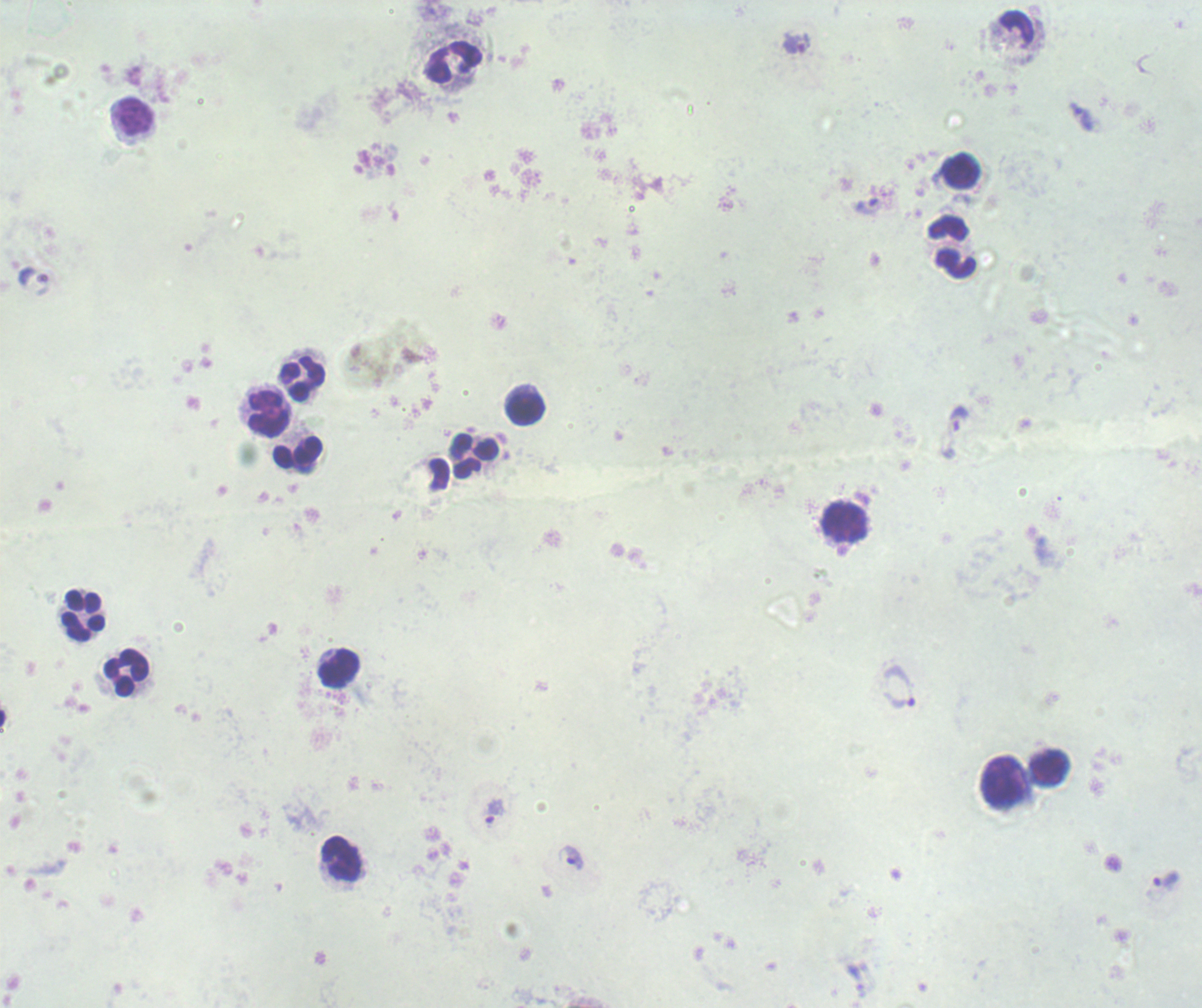

Approximate centers as {x, y} in pixels.
Summary:
  - Leukocyte locations: {453, 62}, {135, 114}, {961, 171}, {949, 228}, {956, 264}, {303, 379}, {526, 409}, {269, 412}, {298, 453}, {476, 455}, {846, 520}, {82, 614}, {339, 668}, {125, 672}, {1050, 769}, {1003, 782}, {341, 858}
  - Trophozoite locations: {797, 44}, {1082, 116}, {866, 206}, {959, 418}, {898, 686}, {494, 812}, {571, 858}, {1165, 880}
  - Image size: 1202×1008 pixels
  - Preparation: thick blood smear
  - Background quality: unsatisfactory
  - Stain: Romanowsky
  - Field of view: single
  - Magnification: 100x
  - Result: positive for Plasmodium parasites
  - Context: previously used in an actual diagnosis